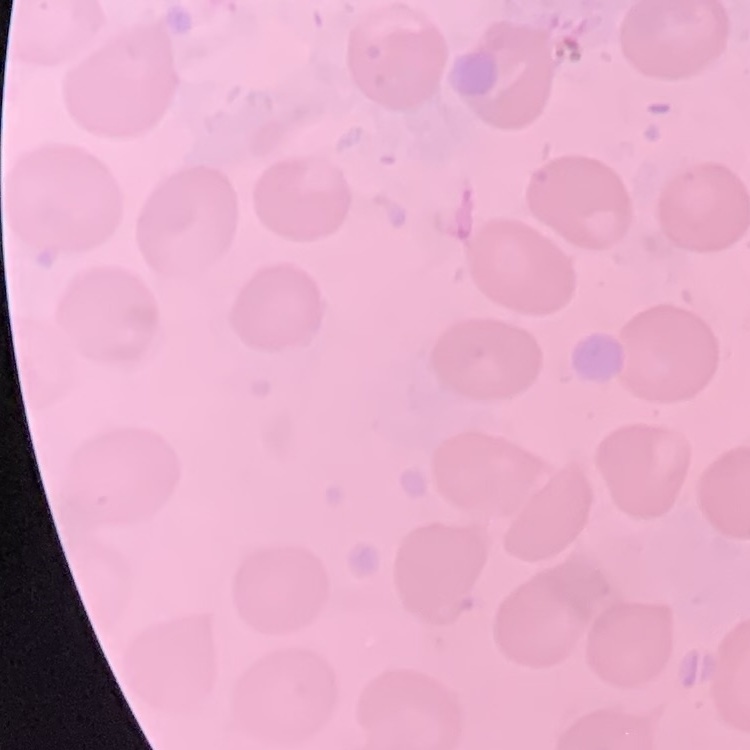

The red blood cells exhibit no rouleaux formation. Square crop of a larger photomicrograph. Thin peripheral smear. Field's or Giemsa stain.